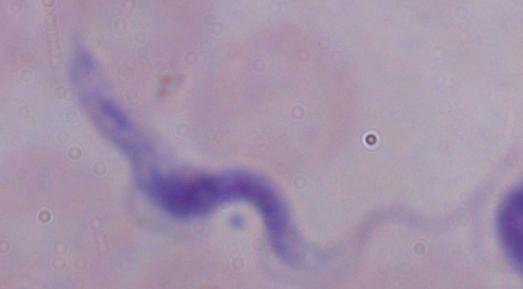
A trypanosome is shown. Photomicrograph. 1000x magnification.